Classify this cell by malaria status.
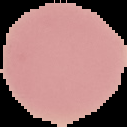

Uninfected.

Image is 127×127 pixels. From a thin blood film. Segmented cell region on a black background.